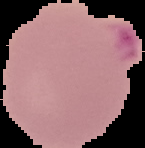

preparation: thin blood smear
image_type: cell region segmented out of the field of view; surrounding area masked to black
image_size: 145×148 pixels
result: malaria parasites detected